Report the malaria status of this cell.
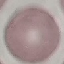
Uninfected.

capture = smartphone through the microscope eyepiece
stain = Giemsa
preparation = thin smear
image type = cell patch, automatically extracted from a larger field of view and resized to 64 × 64 pixels